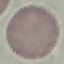

Summary:
  - Result: no malaria parasites detected
  - Stain: Giemsa
  - Image type: automatically extracted cell patch, resized to 64 × 64 pixels
  - Preparation: thin smear
  - Capture: smartphone camera at the microscope eyepiece